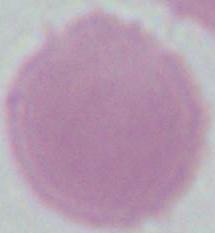
1000x magnification. An erythrocyte is seen. Photomicrograph.